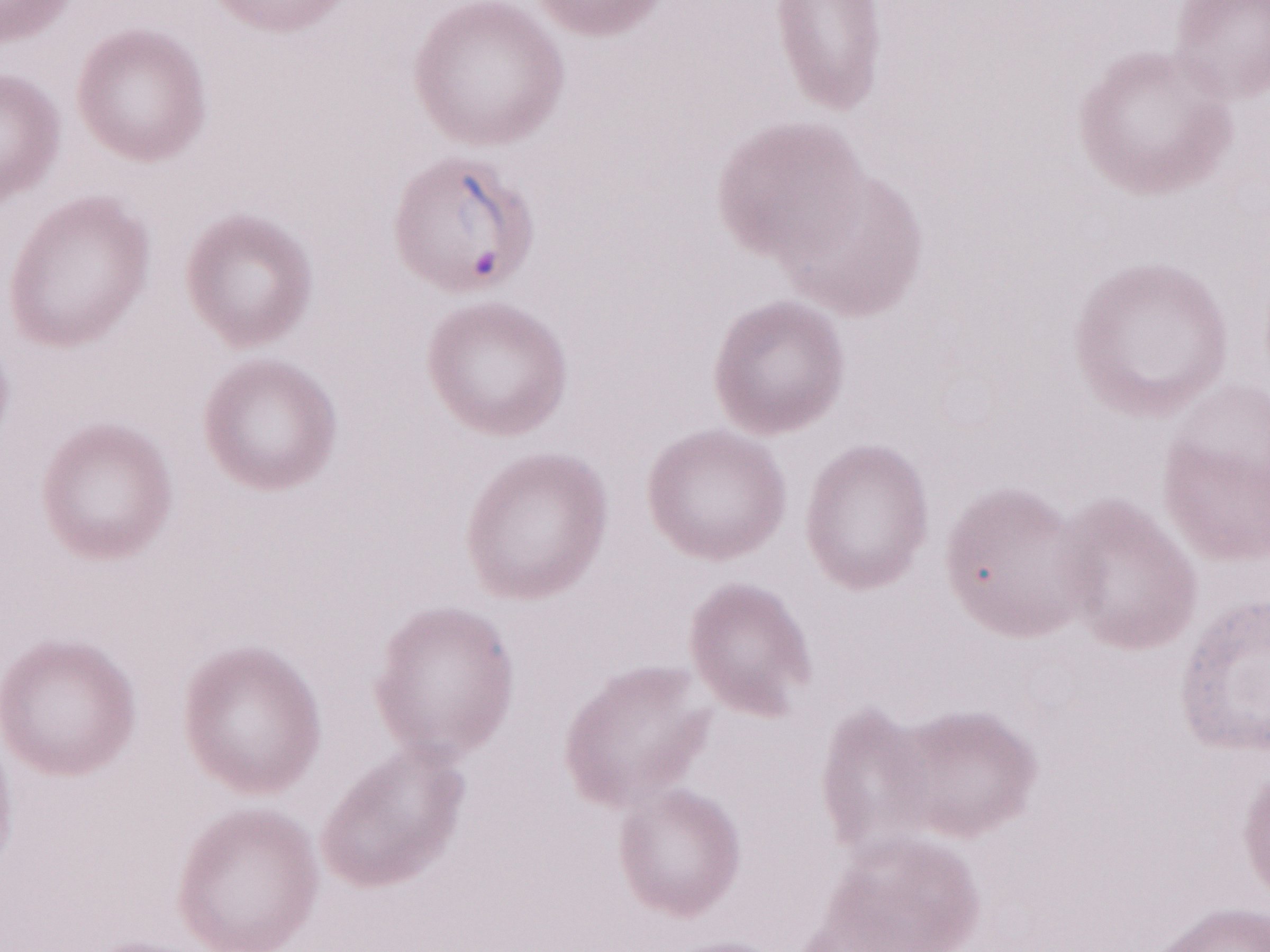

Magnification: 1,000x. One field of this slide. May-Grünwald-Giemsa stain. Image is 1270×952 pixels. Patient-level malaria diagnosis: positive. Thin blood smear. Olympus BX43 microscope and DP73 digital camera.